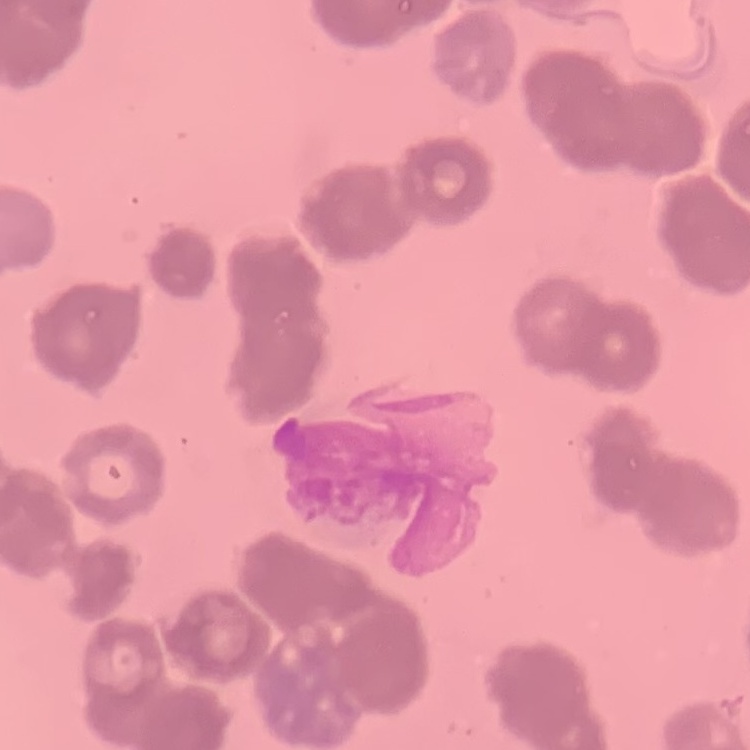
The erythrocytes show rouleaux formation. Square crop of a larger photomicrograph. Field's or Giemsa stain. Thin peripheral smear.